State which parasite is depicted.
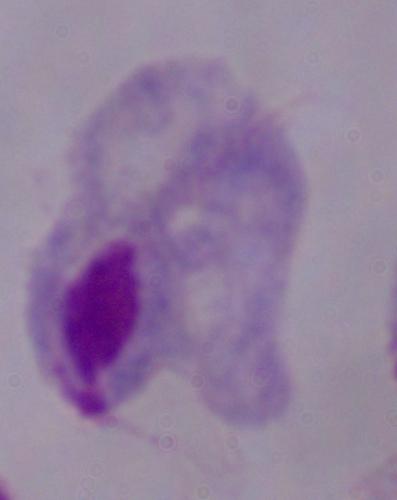

This is a trichomonad.

1000x magnification. Photomicrograph.